Name the parasite shown.
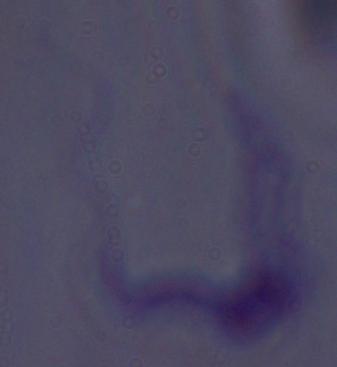
This is a trypanosome.

Micrograph. Captured at 1000x magnification.